Give the extent of all Trypanosoma brucei.
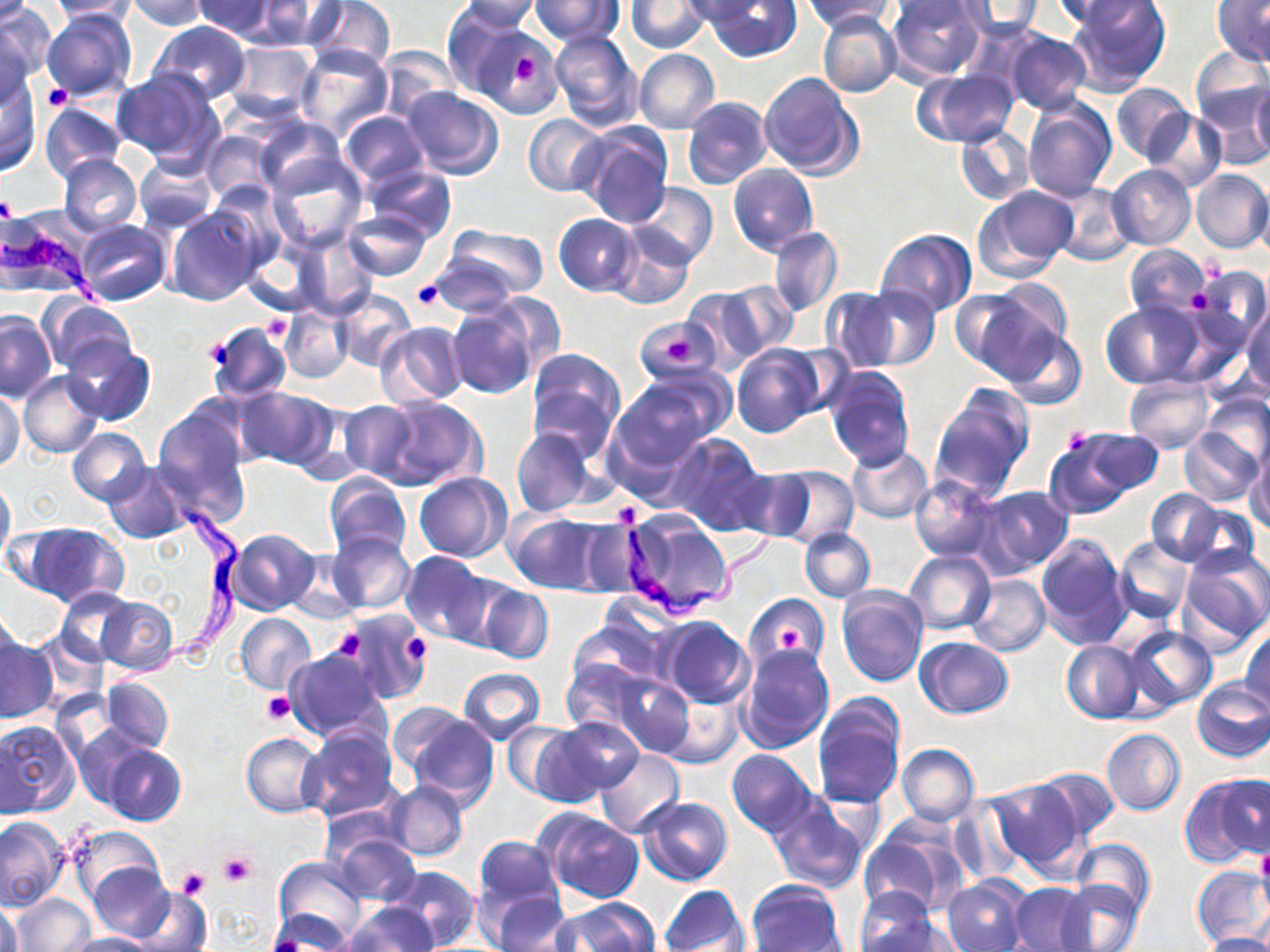
Approximate bounding boxes as named x1/y1/x2/y2 corners in pixels.
Trypanosoma brucei: (x1=1, y1=228, x2=103, y2=304), (x1=119, y1=496, x2=251, y2=677), (x1=612, y1=496, x2=786, y2=631).

Summary:
  - Platelet locations: (x1=512, y1=55, x2=540, y2=83), (x1=44, y1=85, x2=72, y2=112), (x1=0, y1=195, x2=17, y2=226), (x1=411, y1=280, x2=447, y2=310), (x1=1190, y1=290, x2=1211, y2=313), (x1=264, y1=316, x2=291, y2=340), (x1=667, y1=336, x2=697, y2=365), (x1=200, y1=339, x2=235, y2=369), (x1=1062, y1=427, x2=1092, y2=456), (x1=775, y1=625, x2=805, y2=650), (x1=330, y1=629, x2=364, y2=661), (x1=402, y1=633, x2=433, y2=666), (x1=263, y1=692, x2=295, y2=724), (x1=1256, y1=850, x2=1270, y2=891), (x1=217, y1=852, x2=257, y2=887), (x1=176, y1=868, x2=210, y2=901)
  - Uninfected red blood cell locations: (x1=0, y1=0, x2=54, y2=85), (x1=126, y1=0, x2=208, y2=31), (x1=191, y1=0, x2=277, y2=40), (x1=307, y1=0, x2=395, y2=71), (x1=530, y1=0, x2=623, y2=46), (x1=677, y1=0, x2=768, y2=24), (x1=705, y1=0, x2=804, y2=62), (x1=802, y1=0, x2=896, y2=31), (x1=886, y1=0, x2=989, y2=83), (x1=1052, y1=0, x2=1156, y2=32), (x1=1066, y1=0, x2=1172, y2=92), (x1=1213, y1=0, x2=1270, y2=67), (x1=45, y1=1, x2=140, y2=21), (x1=250, y1=1, x2=345, y2=51), (x1=453, y1=1, x2=541, y2=34), (x1=626, y1=1, x2=710, y2=53), (x1=954, y1=1, x2=1042, y2=39), (x1=440, y1=4, x2=528, y2=98), (x1=42, y1=7, x2=137, y2=101), (x1=818, y1=12, x2=901, y2=97), (x1=147, y1=21, x2=251, y2=105), (x1=0, y1=22, x2=38, y2=112), (x1=477, y1=30, x2=559, y2=118), (x1=549, y1=30, x2=642, y2=132), (x1=1004, y1=30, x2=1092, y2=116), (x1=223, y1=40, x2=317, y2=119), (x1=294, y1=44, x2=393, y2=141), (x1=377, y1=44, x2=460, y2=123), (x1=1189, y1=47, x2=1270, y2=131), (x1=634, y1=49, x2=719, y2=134), (x1=112, y1=69, x2=222, y2=166), (x1=915, y1=69, x2=1017, y2=148), (x1=759, y1=72, x2=861, y2=179), (x1=0, y1=75, x2=42, y2=176), (x1=1111, y1=82, x2=1195, y2=164), (x1=1197, y1=83, x2=1269, y2=168), (x1=1249, y1=83, x2=1270, y2=162), (x1=398, y1=86, x2=505, y2=179), (x1=683, y1=97, x2=771, y2=189), (x1=1023, y1=99, x2=1115, y2=200), (x1=39, y1=102, x2=126, y2=181), (x1=339, y1=110, x2=428, y2=188), (x1=1146, y1=110, x2=1227, y2=193), (x1=523, y1=114, x2=608, y2=196), (x1=253, y1=117, x2=347, y2=198), (x1=579, y1=124, x2=672, y2=226), (x1=955, y1=127, x2=1035, y2=205), (x1=201, y1=129, x2=280, y2=208), (x1=58, y1=153, x2=143, y2=239), (x1=134, y1=154, x2=218, y2=231), (x1=266, y1=155, x2=368, y2=252), (x1=364, y1=164, x2=457, y2=243), (x1=728, y1=164, x2=818, y2=256), (x1=1107, y1=164, x2=1196, y2=250), (x1=1190, y1=169, x2=1270, y2=253), (x1=1251, y1=180, x2=1270, y2=262), (x1=631, y1=183, x2=717, y2=267), (x1=1049, y1=183, x2=1134, y2=264), (x1=974, y1=186, x2=1077, y2=282), (x1=168, y1=206, x2=262, y2=307), (x1=344, y1=210, x2=433, y2=280), (x1=553, y1=214, x2=641, y2=296), (x1=74, y1=219, x2=171, y2=307), (x1=447, y1=224, x2=549, y2=300), (x1=609, y1=224, x2=696, y2=310), (x1=768, y1=227, x2=844, y2=318), (x1=877, y1=229, x2=976, y2=317), (x1=294, y1=232, x2=378, y2=317), (x1=240, y1=241, x2=323, y2=318), (x1=1123, y1=245, x2=1214, y2=321), (x1=429, y1=249, x2=526, y2=316), (x1=1189, y1=266, x2=1268, y2=345), (x1=715, y1=280, x2=799, y2=360), (x1=851, y1=285, x2=940, y2=370), (x1=953, y1=286, x2=1064, y2=380), (x1=822, y1=287, x2=903, y2=371), (x1=680, y1=288, x2=770, y2=369), (x1=334, y1=291, x2=415, y2=372), (x1=484, y1=292, x2=564, y2=378), (x1=41, y1=298, x2=136, y2=376), (x1=1100, y1=301, x2=1203, y2=389), (x1=447, y1=302, x2=540, y2=398), (x1=280, y1=304, x2=354, y2=383), (x1=1242, y1=304, x2=1270, y2=395), (x1=0, y1=312, x2=55, y2=404), (x1=207, y1=322, x2=292, y2=403), (x1=375, y1=322, x2=467, y2=408), (x1=1001, y1=329, x2=1087, y2=411), (x1=64, y1=338, x2=153, y2=424), (x1=732, y1=344, x2=825, y2=438), (x1=525, y1=348, x2=626, y2=459), (x1=824, y1=367, x2=914, y2=470), (x1=19, y1=371, x2=103, y2=459), (x1=612, y1=373, x2=724, y2=467), (x1=1123, y1=377, x2=1215, y2=452), (x1=234, y1=386, x2=335, y2=471), (x1=930, y1=386, x2=1034, y2=501), (x1=1, y1=390, x2=25, y2=472), (x1=1199, y1=393, x2=1270, y2=469), (x1=374, y1=396, x2=485, y2=491), (x1=152, y1=401, x2=251, y2=515), (x1=335, y1=401, x2=419, y2=482), (x1=68, y1=427, x2=149, y2=506), (x1=511, y1=428, x2=595, y2=517), (x1=1179, y1=428, x2=1264, y2=507), (x1=1044, y1=429, x2=1151, y2=519), (x1=666, y1=433, x2=767, y2=532), (x1=1246, y1=443, x2=1270, y2=534), (x1=847, y1=444, x2=934, y2=523), (x1=103, y1=461, x2=192, y2=542), (x1=772, y1=465, x2=859, y2=547), (x1=730, y1=466, x2=815, y2=541), (x1=415, y1=472, x2=510, y2=562), (x1=0, y1=474, x2=15, y2=569), (x1=325, y1=474, x2=411, y2=561), (x1=910, y1=474, x2=999, y2=561), (x1=975, y1=484, x2=1074, y2=576), (x1=1148, y1=489, x2=1224, y2=564), (x1=1176, y1=501, x2=1260, y2=574), (x1=505, y1=510, x2=604, y2=595), (x1=621, y1=511, x2=734, y2=618), (x1=576, y1=518, x2=648, y2=597), (x1=24, y1=523, x2=129, y2=609), (x1=799, y1=528, x2=874, y2=601), (x1=227, y1=529, x2=318, y2=614), (x1=328, y1=533, x2=415, y2=615), (x1=1035, y1=533, x2=1133, y2=650), (x1=1114, y1=536, x2=1194, y2=624), (x1=1177, y1=547, x2=1270, y2=652), (x1=286, y1=549, x2=366, y2=621), (x1=904, y1=549, x2=994, y2=635), (x1=401, y1=551, x2=489, y2=642), (x1=441, y1=572, x2=519, y2=655), (x1=965, y1=575, x2=1050, y2=657), (x1=477, y1=584, x2=553, y2=664), (x1=55, y1=586, x2=135, y2=666), (x1=837, y1=588, x2=929, y2=689), (x1=746, y1=594, x2=830, y2=669), (x1=96, y1=596, x2=178, y2=674), (x1=0, y1=607, x2=20, y2=685), (x1=342, y1=609, x2=428, y2=702), (x1=236, y1=613, x2=316, y2=695), (x1=659, y1=617, x2=754, y2=709), (x1=568, y1=620, x2=661, y2=696), (x1=1241, y1=625, x2=1270, y2=713), (x1=1123, y1=627, x2=1218, y2=714), (x1=0, y1=637, x2=57, y2=724), (x1=915, y1=637, x2=1014, y2=718), (x1=1061, y1=640, x2=1144, y2=723), (x1=739, y1=643, x2=834, y2=755), (x1=283, y1=648, x2=387, y2=742), (x1=562, y1=655, x2=656, y2=734), (x1=457, y1=667, x2=546, y2=745), (x1=613, y1=672, x2=695, y2=760), (x1=101, y1=677, x2=173, y2=753), (x1=1192, y1=678, x2=1270, y2=762), (x1=659, y1=691, x2=744, y2=767), (x1=813, y1=698, x2=905, y2=808), (x1=387, y1=701, x2=473, y2=780), (x1=405, y1=711, x2=498, y2=808), (x1=549, y1=716, x2=647, y2=799), (x1=0, y1=720, x2=81, y2=815), (x1=501, y1=722, x2=578, y2=798), (x1=301, y1=725, x2=399, y2=820), (x1=526, y1=725, x2=612, y2=807), (x1=74, y1=726, x2=152, y2=809), (x1=1102, y1=728, x2=1185, y2=815), (x1=241, y1=732, x2=324, y2=816), (x1=897, y1=744, x2=978, y2=825), (x1=102, y1=745, x2=186, y2=826), (x1=595, y1=749, x2=685, y2=837), (x1=726, y1=749, x2=817, y2=835), (x1=1035, y1=767, x2=1119, y2=839), (x1=1181, y1=771, x2=1269, y2=867), (x1=987, y1=777, x2=1091, y2=879), (x1=388, y1=781, x2=467, y2=862), (x1=766, y1=794, x2=868, y2=895), (x1=639, y1=796, x2=732, y2=886), (x1=948, y1=796, x2=1029, y2=885), (x1=538, y1=810, x2=645, y2=903), (x1=0, y1=816, x2=69, y2=910), (x1=857, y1=819, x2=966, y2=919), (x1=68, y1=826, x2=164, y2=906), (x1=331, y1=833, x2=421, y2=905), (x1=473, y1=836, x2=562, y2=913), (x1=1071, y1=837, x2=1156, y2=917), (x1=274, y1=857, x2=368, y2=946), (x1=86, y1=862, x2=177, y2=943), (x1=387, y1=866, x2=478, y2=949), (x1=1191, y1=866, x2=1270, y2=950), (x1=855, y1=871, x2=946, y2=948), (x1=942, y1=876, x2=1030, y2=952), (x1=747, y1=880, x2=845, y2=952), (x1=1059, y1=880, x2=1143, y2=952), (x1=659, y1=884, x2=749, y2=952), (x1=1008, y1=884, x2=1093, y2=950), (x1=127, y1=886, x2=210, y2=952), (x1=483, y1=888, x2=573, y2=952), (x1=10, y1=894, x2=94, y2=952), (x1=1, y1=899, x2=23, y2=952), (x1=553, y1=899, x2=658, y2=952), (x1=343, y1=902, x2=438, y2=951), (x1=266, y1=906, x2=356, y2=951), (x1=860, y1=911, x2=957, y2=952), (x1=61, y1=932, x2=156, y2=952), (x1=1204, y1=932, x2=1269, y2=952)
  - Slide-level diagnosis: Trypanosoma brucei
  - Field of view: single
  - Stain: May-Grünwald-Giemsa
  - Modality: optical microscopy
  - Image size: 1270×952 pixels
  - Magnification: 1000x
  - Preparation: thin blood smear